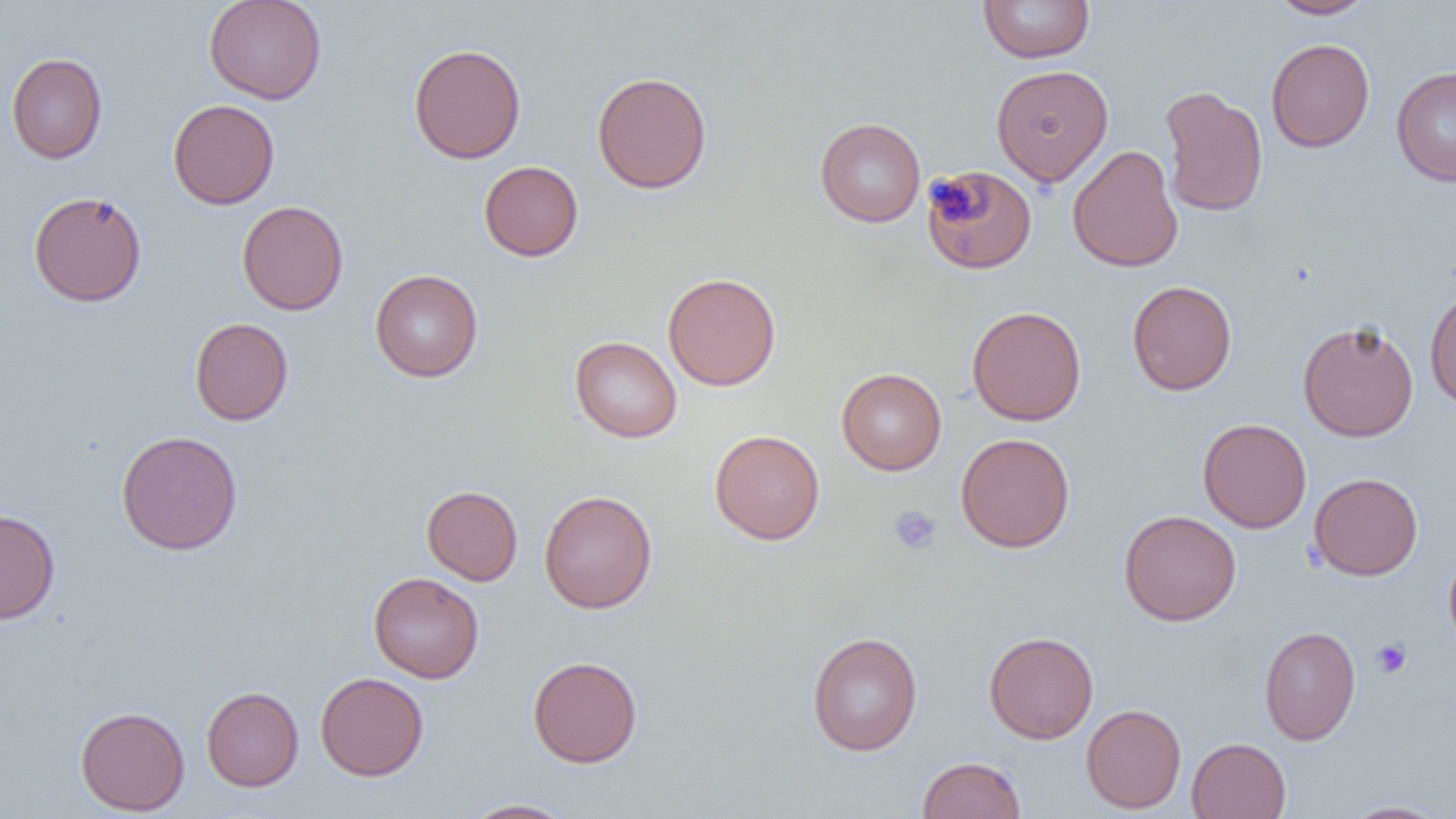
Summary:
  - Coordinate format: approximate bounding boxes as [x1, y1, x2, y2] in pixels
  - Uninfected red blood cell locations: [203, 0, 328, 104], [977, 0, 1095, 63], [1266, 0, 1375, 19], [1266, 38, 1375, 152], [409, 43, 526, 164], [6, 52, 108, 164], [991, 64, 1113, 186], [1391, 65, 1456, 187], [592, 71, 712, 194], [1159, 85, 1268, 217], [167, 99, 280, 209], [815, 117, 926, 227], [1067, 144, 1184, 273], [479, 160, 584, 261], [922, 164, 1037, 274], [28, 191, 147, 308], [237, 200, 349, 315], [369, 269, 483, 382], [663, 272, 781, 390], [1127, 280, 1237, 396], [1424, 285, 1456, 410], [967, 306, 1086, 425], [190, 317, 293, 425], [1297, 320, 1419, 442], [569, 336, 682, 443], [836, 367, 947, 475], [1198, 418, 1311, 533], [709, 429, 825, 545], [115, 430, 243, 555], [955, 433, 1075, 552], [1309, 472, 1423, 580], [422, 485, 523, 585], [539, 490, 658, 614], [0, 508, 61, 624], [1118, 510, 1241, 626], [1443, 546, 1456, 654], [368, 572, 484, 683], [1259, 625, 1361, 745], [807, 631, 923, 756], [983, 631, 1099, 744], [528, 655, 642, 768], [315, 672, 429, 780], [201, 686, 304, 791], [1080, 704, 1186, 813], [75, 706, 190, 815], [1186, 737, 1291, 818], [917, 756, 1025, 818], [460, 798, 576, 818], [1339, 800, 1450, 818]
  - Platelet locations: [889, 505, 942, 554], [1371, 638, 1411, 678]
  - Slide-level diagnosis: negative for blood parasites
  - Image size: 1456×819 pixels
  - Field of view: one of a larger specimen
  - Preparation: thin blood film
  - Modality: light microscopy
  - Magnification: 1000x